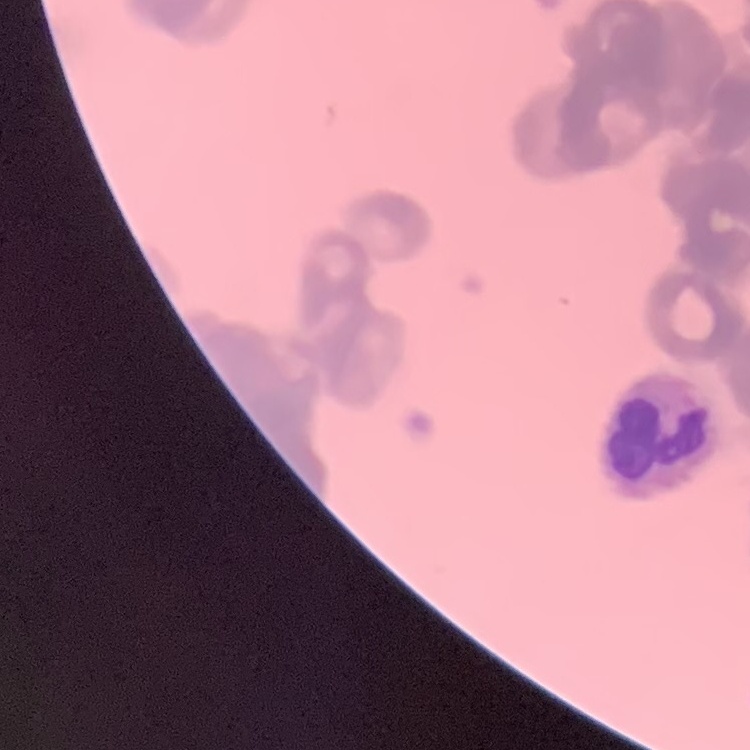

Summary:
  - Red blood cell morphology: rouleaux formation
  - Image type: square crop of a larger photomicrograph
  - Preparation: thin blood film
  - Stain: Field's or Giemsa